Assess the morphology of the red blood cells.
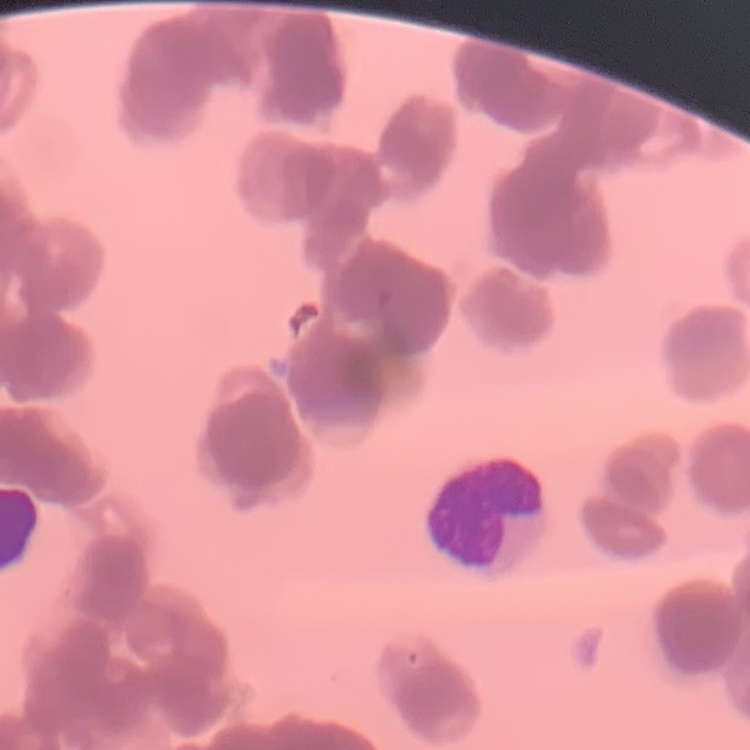

Rouleaux formation.

Thin blood smear. Stained with either Field's or Giemsa. One tile cut from a larger photomicrograph.